Evaluate for malaria.
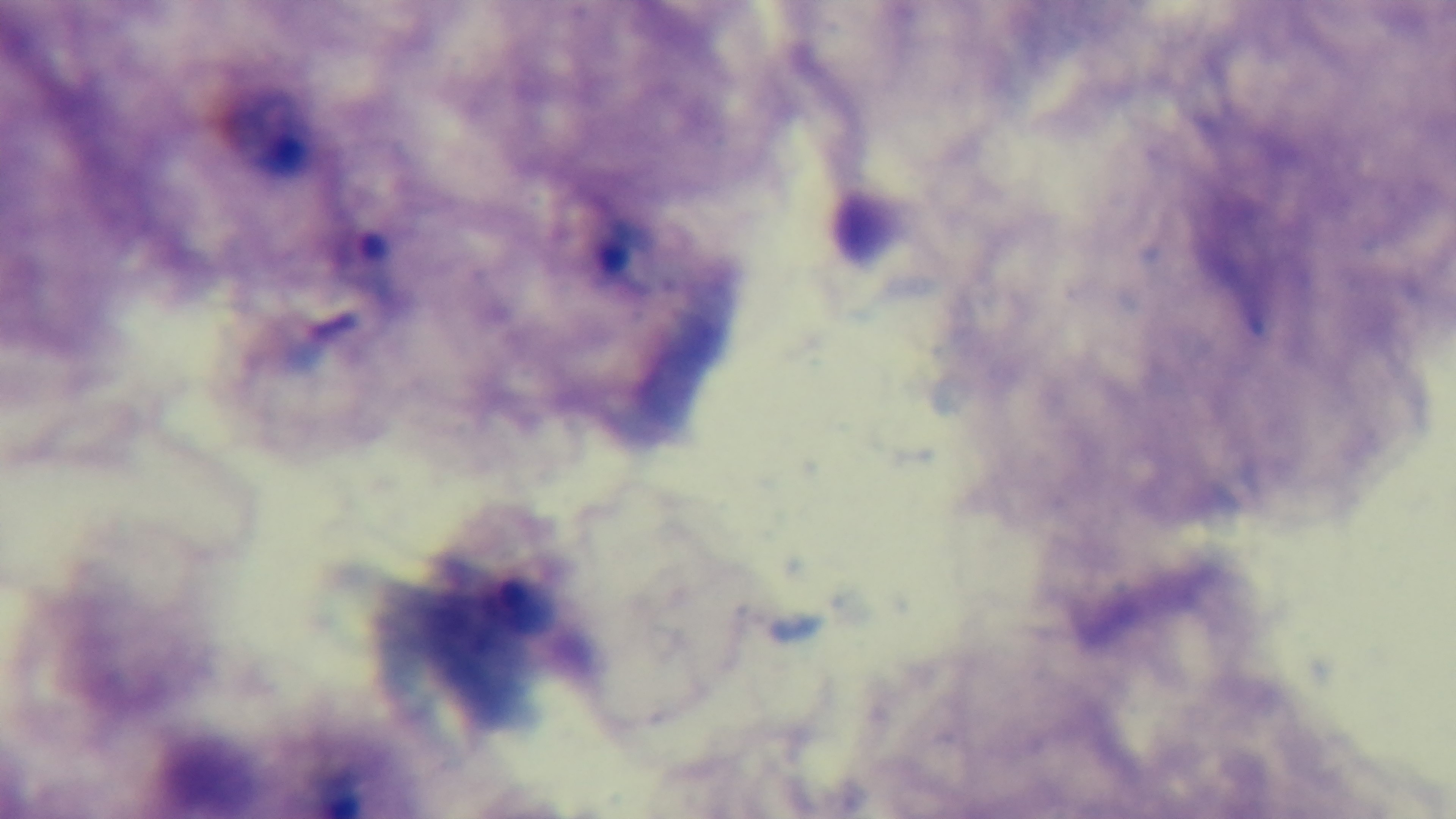
Infected.

100x oil-immersion objective. Preparation: thick. Giemsa stain. Single field of view. Captured with a mounted 4K digital camera. Light microscopy.